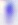

Summary:
  - Identification: Toxoplasma gondii
  - Modality: micrograph
  - Magnification: 400x